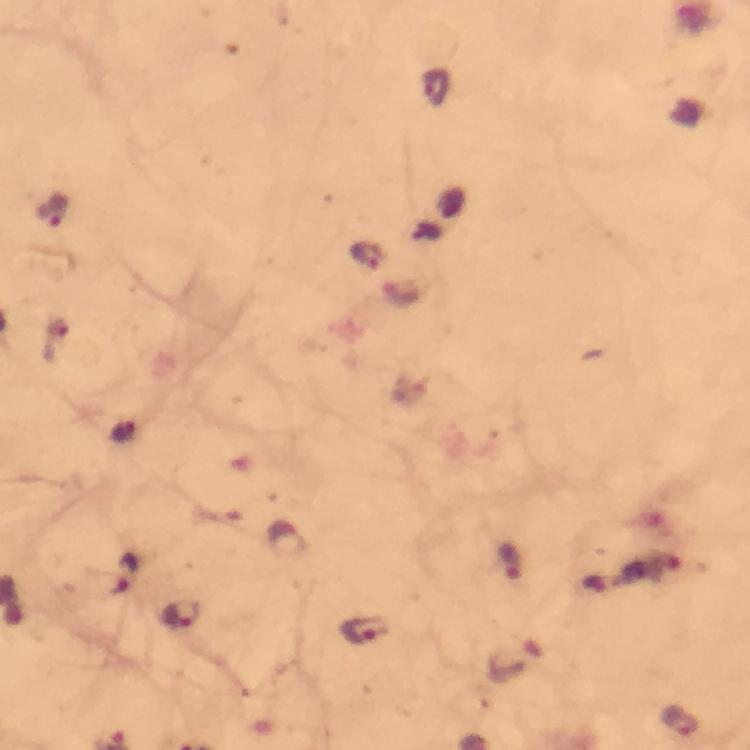

{
  "context": "from a diagnostic examination for malaria",
  "image_size": "750×750 pixels",
  "immersion_oil": "applied",
  "plasmodium_parasite_locations": "approximate centers as [x, y] in pixels: [437, 87], [54, 209], [367, 255], [124, 431], [511, 561], [127, 571], [182, 616], [365, 630], [680, 720]",
  "stain": "Giemsa",
  "capture": "smartphone camera through the microscope",
  "cropped_from": "a single field of view",
  "preparation": "thick smear",
  "magnification": "100x"
}